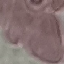
{
  "result": "no malaria parasites detected",
  "preparation": "thin blood smear",
  "capture": "smartphone camera at the microscope eyepiece",
  "stain": "Giemsa",
  "image_type": "automatically extracted cell patch, resized to 64 × 64 pixels"
}